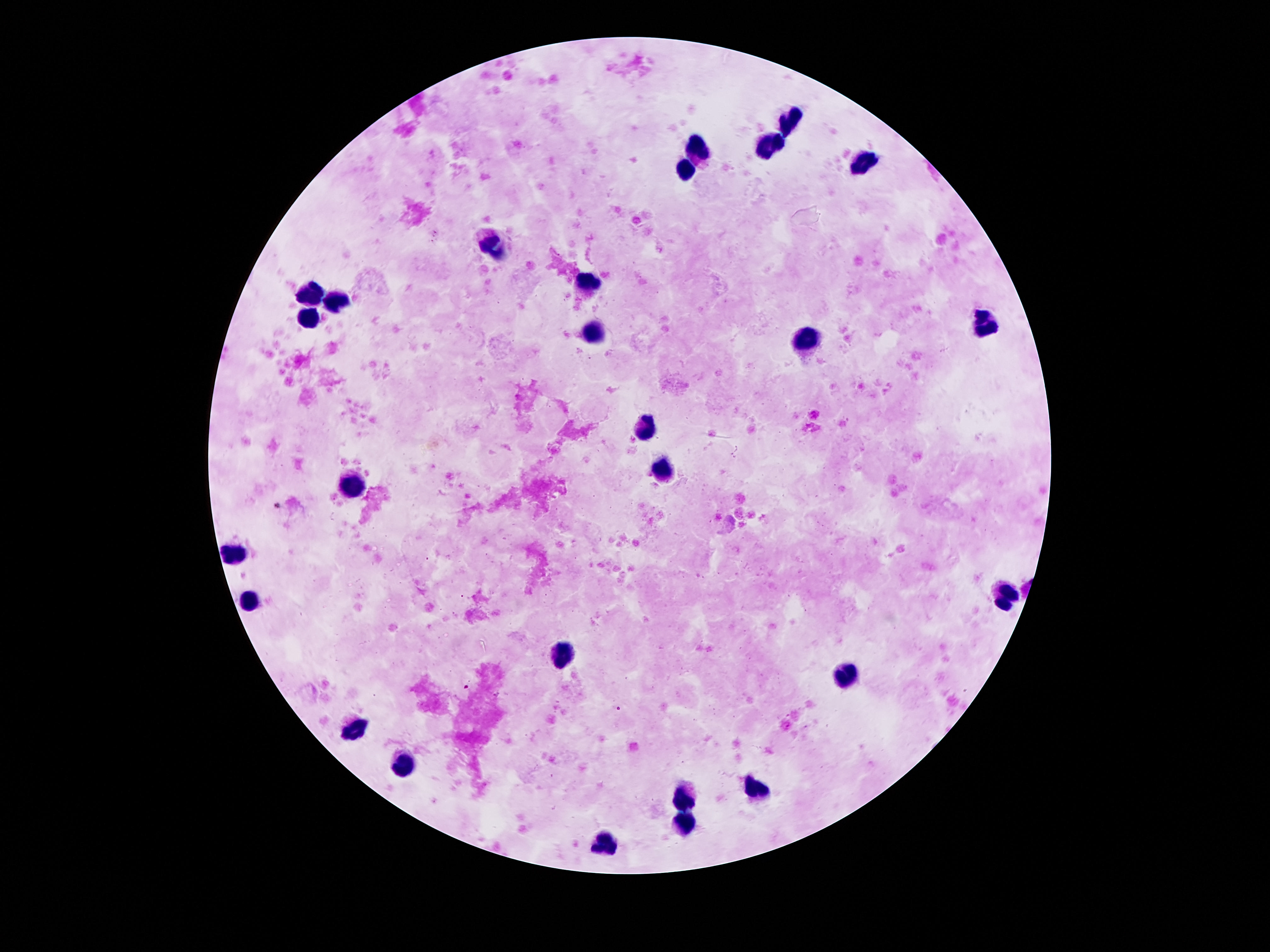

Approximate centers as {x, y} in pixels.
Summary:
  - Leukocyte locations: {790, 121}, {768, 143}, {697, 147}, {863, 162}, {682, 169}, {497, 246}, {590, 277}, {310, 296}, {338, 300}, {308, 320}, {988, 320}, {599, 333}, {807, 339}, {644, 421}, {665, 470}, {353, 485}, {232, 552}, {1003, 597}, {248, 600}, {562, 660}, {850, 679}, {355, 727}, {400, 766}, {754, 789}, {687, 800}, {685, 824}, {603, 845}
  - Capture: smartphone camera through the microscope eyepiece
  - Preparation: thick blood smear
  - Field of view: single
  - Image size: 1270×952 pixels
  - Magnification: 100x
  - Patient malaria status: negative
  - Stain: Giemsa